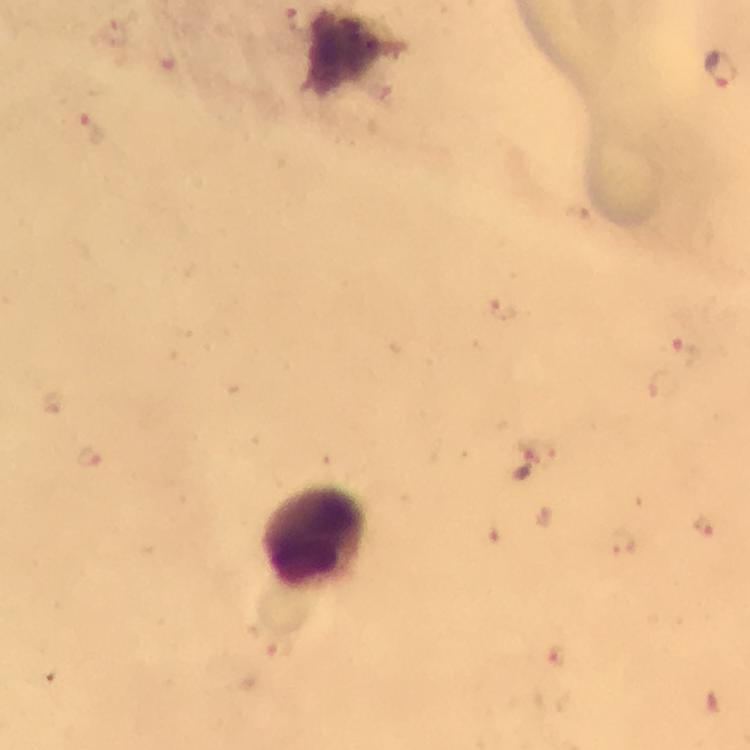

{
  "stain": "Giemsa",
  "preparation": "thick blood smear",
  "immersion_oil": "used",
  "magnification": "100x",
  "cropped_from": "one field of view",
  "capture": "smartphone photograph through a microscope",
  "context": "from a malaria diagnostic workup",
  "leukocyte_locations": "approximate centers as {x, y} in pixels: {316, 538}",
  "malaria_parasite_locations": "approximate centers as {x, y} in pixels: {301, 24}, {718, 67}, {89, 128}, {504, 308}, {687, 347}, {91, 455}, {534, 463}, {704, 526}, {624, 545}, {282, 652}, {559, 656}",
  "image_size": "750×750 pixels"
}